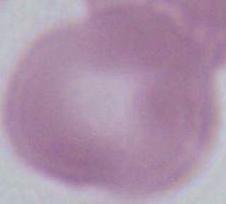
Summary:
  - Identification: erythrocyte
  - Magnification: 1000x
  - Modality: photomicrograph